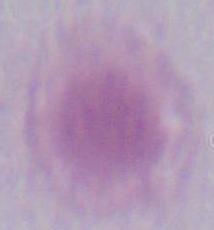
A red blood cell is shown. Captured at 1000x magnification. Micrograph.